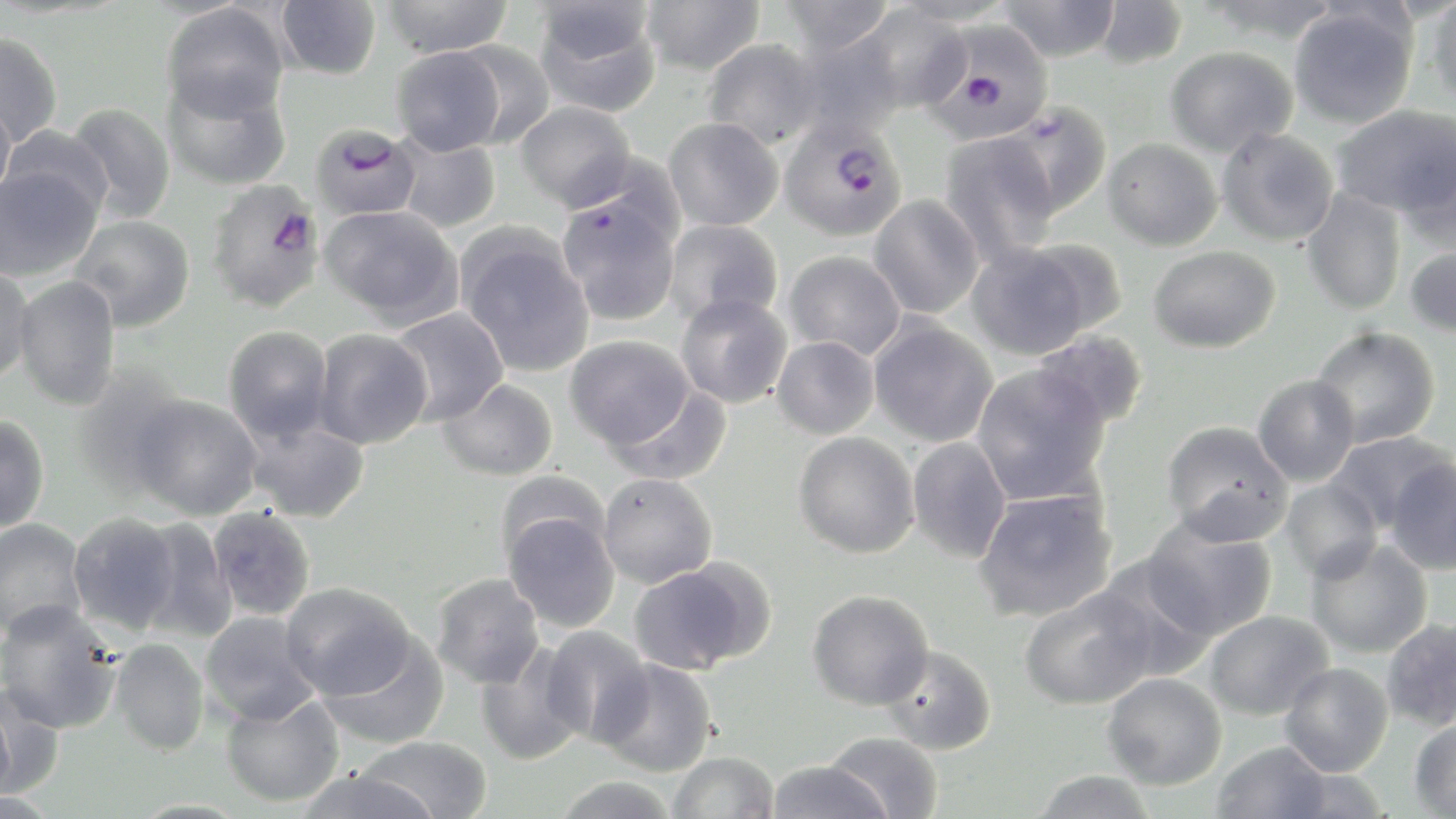

Approximate bounding boxes as (x1, y1, x2, y2) in pixels. Plasmodium falciparum-infected red blood cell locations: (930, 21, 1054, 142), (780, 117, 907, 241), (310, 123, 421, 222), (205, 179, 327, 312). Uninfected red blood cell locations: (378, 0, 514, 58), (640, 0, 764, 76), (775, 0, 895, 56), (891, 0, 1016, 26), (1202, 0, 1344, 43), (1425, 0, 1456, 108), (274, 1, 381, 80), (533, 1, 661, 117), (997, 1, 1121, 61), (1093, 1, 1188, 69), (161, 3, 289, 121), (1288, 4, 1419, 129), (853, 5, 971, 115), (791, 29, 907, 140), (0, 32, 63, 148), (451, 40, 556, 149), (701, 40, 824, 150), (1165, 45, 1298, 157), (392, 46, 506, 156), (162, 73, 292, 191), (0, 98, 16, 205), (515, 101, 636, 210), (999, 101, 1113, 220), (64, 103, 176, 224), (1332, 105, 1456, 217), (663, 117, 783, 231), (2, 124, 112, 222), (1217, 128, 1339, 246), (392, 132, 501, 234), (939, 133, 1061, 265), (1102, 138, 1223, 251), (1396, 146, 1456, 256), (0, 164, 103, 281), (556, 187, 681, 327), (1302, 189, 1407, 316), (868, 195, 984, 319), (318, 204, 464, 328), (67, 214, 196, 331), (664, 218, 784, 326), (456, 228, 594, 377), (1022, 237, 1127, 339), (966, 242, 1097, 360), (1404, 244, 1456, 338), (1148, 245, 1281, 353), (783, 251, 905, 360), (0, 263, 34, 386), (12, 275, 122, 411), (675, 292, 792, 409), (387, 308, 509, 427), (868, 317, 999, 447), (223, 325, 334, 443), (1310, 326, 1441, 448), (312, 328, 432, 450), (1031, 331, 1150, 431), (565, 335, 694, 449), (771, 337, 880, 439), (971, 364, 1111, 505), (70, 365, 192, 495), (1252, 374, 1360, 486), (437, 377, 558, 481), (608, 384, 733, 486), (127, 394, 263, 521), (0, 413, 50, 533), (244, 416, 371, 524), (1160, 420, 1293, 546), (1327, 431, 1454, 532), (793, 432, 919, 558), (907, 437, 1012, 563), (1385, 458, 1456, 574), (495, 470, 610, 566), (598, 473, 718, 589), (1280, 479, 1383, 582), (973, 489, 1118, 622), (207, 506, 317, 621), (502, 510, 621, 632), (68, 512, 183, 636), (1141, 516, 1278, 640), (0, 518, 89, 638), (133, 518, 237, 642), (1305, 537, 1433, 659), (1093, 556, 1217, 679), (628, 558, 773, 675), (431, 572, 545, 689), (280, 581, 416, 699), (1019, 587, 1156, 710), (806, 589, 934, 709), (0, 601, 120, 735), (1203, 610, 1334, 720), (200, 611, 321, 726), (1381, 618, 1456, 733), (541, 627, 654, 747), (318, 632, 450, 750), (110, 637, 209, 756), (474, 643, 589, 765), (878, 644, 997, 755), (597, 658, 718, 776), (1279, 662, 1394, 777), (1102, 673, 1227, 790), (0, 682, 63, 800), (0, 687, 17, 809), (220, 691, 345, 807), (1409, 716, 1456, 817), (824, 731, 944, 818), (360, 736, 492, 819), (1211, 741, 1332, 818), (668, 751, 780, 818), (766, 759, 892, 818), (293, 767, 441, 819), (1031, 769, 1157, 818), (552, 776, 680, 819). Slide-level diagnosis: Plasmodium falciparum. 1000x magnification. Light microscopy. Image is 1456×819 pixels. May-Grünwald-Giemsa-stained preparation. One field of a larger specimen. Thin blood film.